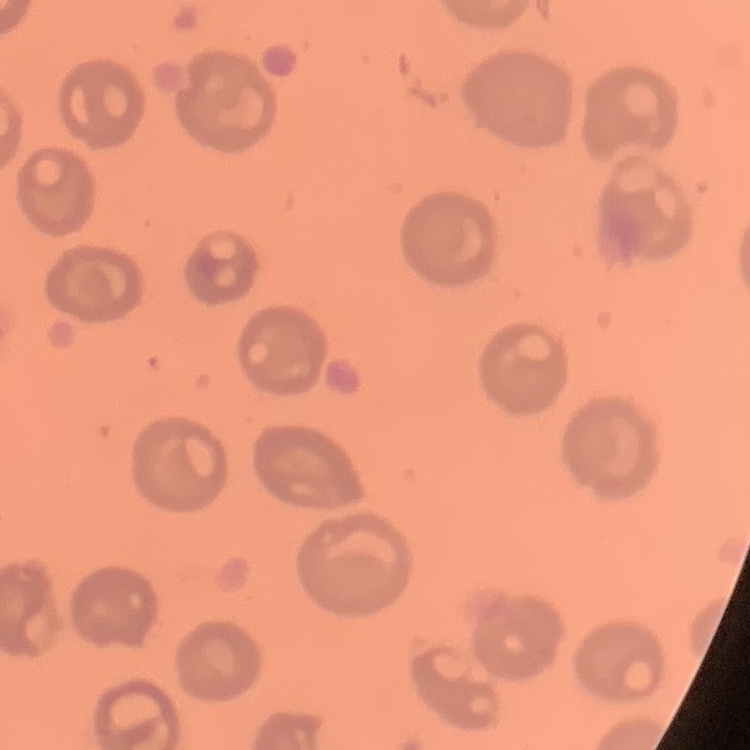

red_blood_cell_morphology: no rouleaux formation
preparation: thin peripheral smear
image_type: square crop of a larger photomicrograph
stain: Field's or Giemsa